Report the malaria status of this cell.
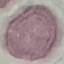
It is uninfected.

capture = smartphone camera at the microscope eyepiece
stain = Giemsa
preparation = thin blood film
image type = automatically extracted cell patch, resized to 64 × 64 pixels